Locate and identify every blood parasite.
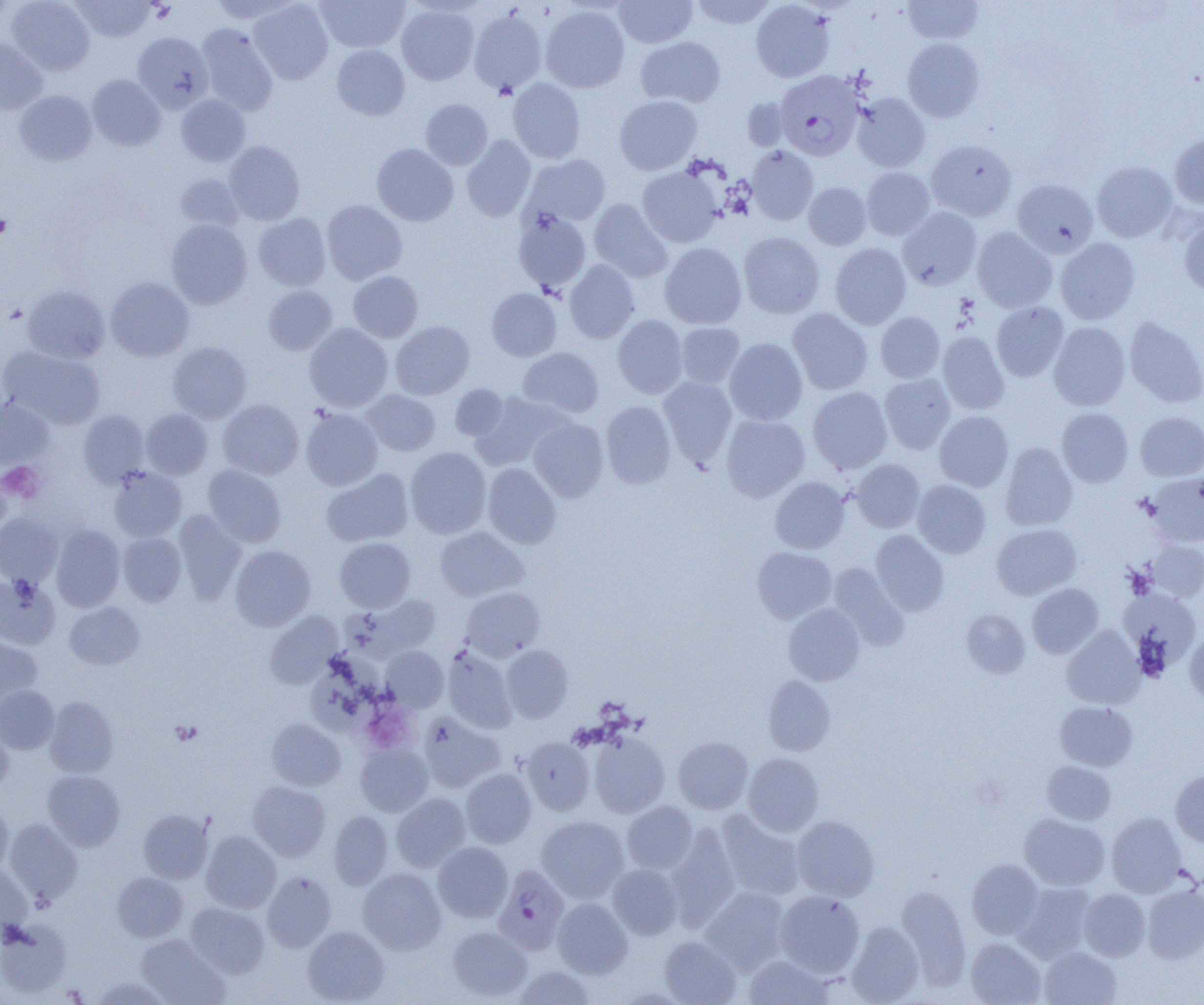
Approximate bounding boxes as [x1, y1, x2, y2] in pixels.
Plasmodium falciparum-infected red blood cells: [778, 76, 867, 165], [493, 865, 570, 954].
No Plasmodium ovale, Plasmodium malariae, Plasmodium vivax, Babesia divergens, or Trypanosoma brucei observed.

Summary:
  - Platelet locations: [149, 2, 175, 21], [0, 213, 11, 240], [1, 461, 44, 502], [169, 719, 203, 746]
  - Uninfected red blood cell locations: [7, 0, 95, 75], [71, 0, 155, 42], [209, 0, 301, 22], [248, 0, 333, 85], [316, 0, 409, 52], [614, 0, 697, 48], [689, 0, 778, 29], [751, 0, 834, 82], [902, 0, 983, 44], [396, 4, 479, 85], [540, 5, 630, 92], [468, 9, 547, 95], [196, 24, 278, 115], [133, 32, 213, 112], [635, 36, 726, 107], [902, 37, 985, 122], [0, 39, 46, 115], [332, 44, 410, 120], [87, 74, 166, 151], [507, 78, 586, 163], [14, 90, 97, 166], [851, 92, 930, 172], [176, 94, 250, 166], [614, 95, 702, 175], [742, 97, 793, 151], [420, 98, 493, 170], [461, 135, 535, 221], [1170, 135, 1204, 208], [224, 140, 305, 225], [926, 140, 1017, 221], [372, 143, 458, 226], [746, 145, 819, 225], [525, 154, 611, 227], [1092, 161, 1177, 242], [637, 166, 723, 247], [862, 167, 935, 240], [175, 174, 245, 232], [1013, 179, 1098, 256], [803, 182, 871, 250], [589, 199, 672, 282], [321, 200, 407, 284], [897, 207, 982, 290], [512, 209, 591, 293], [253, 212, 331, 291], [1179, 218, 1204, 294], [166, 220, 252, 309], [972, 227, 1056, 312], [738, 232, 825, 319], [1056, 237, 1140, 324], [659, 242, 747, 329], [830, 243, 911, 329], [564, 259, 640, 343], [348, 271, 423, 342], [106, 277, 194, 361], [23, 284, 110, 364], [263, 285, 337, 355], [487, 288, 562, 361], [991, 302, 1069, 381], [787, 308, 873, 395], [875, 311, 945, 383], [612, 314, 688, 398], [1124, 316, 1204, 407], [390, 321, 474, 399], [675, 322, 745, 388], [1049, 322, 1130, 411], [304, 323, 393, 412], [937, 332, 1009, 414], [725, 338, 808, 425], [168, 342, 251, 423], [1, 346, 105, 430], [517, 347, 604, 419], [879, 373, 955, 453], [658, 376, 737, 465], [450, 384, 510, 442], [808, 386, 892, 473], [361, 389, 440, 456], [469, 392, 563, 470], [0, 398, 54, 470], [218, 399, 303, 479], [601, 400, 676, 489], [301, 407, 382, 491], [141, 408, 213, 479], [1057, 408, 1133, 487], [78, 410, 149, 486], [934, 411, 1013, 491], [1135, 411, 1204, 481], [721, 414, 809, 502], [529, 417, 609, 502], [1000, 443, 1078, 530], [405, 446, 491, 538], [851, 459, 925, 532], [483, 463, 561, 549], [203, 464, 287, 547], [108, 467, 187, 542], [321, 468, 414, 547], [1145, 473, 1204, 547], [770, 476, 850, 554], [912, 480, 991, 558], [173, 510, 246, 603], [0, 513, 62, 586], [51, 524, 125, 611], [991, 524, 1081, 600], [435, 527, 528, 601], [871, 529, 950, 616], [118, 532, 186, 606], [334, 537, 416, 612], [1145, 540, 1204, 601], [230, 545, 315, 631], [752, 547, 837, 623], [828, 563, 909, 650], [0, 574, 61, 649], [1027, 583, 1103, 658], [461, 587, 545, 661], [1120, 589, 1201, 676], [359, 594, 441, 659], [64, 602, 144, 670], [783, 603, 865, 685], [962, 609, 1030, 678], [265, 611, 343, 687], [1061, 626, 1144, 710], [1185, 629, 1204, 705], [0, 636, 42, 710], [381, 645, 449, 711], [501, 645, 573, 721], [308, 647, 382, 731], [442, 647, 517, 732], [762, 675, 836, 755], [0, 685, 59, 754], [45, 697, 119, 777], [1054, 701, 1138, 771], [419, 712, 505, 793], [266, 719, 345, 790], [0, 724, 13, 796], [588, 731, 670, 818], [673, 736, 753, 814], [521, 737, 595, 815], [356, 743, 433, 816], [744, 753, 823, 836], [1042, 761, 1116, 825], [461, 768, 536, 848], [1170, 768, 1204, 847], [43, 770, 125, 850], [248, 781, 330, 861], [391, 792, 471, 871], [623, 801, 698, 874], [0, 803, 12, 875], [138, 809, 212, 883], [329, 810, 393, 889], [716, 810, 804, 901], [1107, 813, 1186, 897], [1019, 814, 1110, 890], [792, 815, 880, 902], [536, 816, 629, 902], [4, 818, 83, 904], [665, 825, 740, 928], [201, 831, 281, 913], [433, 841, 513, 922], [967, 859, 1043, 939], [0, 864, 33, 937], [608, 864, 683, 939], [358, 868, 445, 954], [112, 872, 188, 942], [262, 872, 336, 952], [1015, 882, 1096, 961], [895, 885, 971, 989], [1142, 885, 1204, 963], [702, 886, 791, 973], [1079, 888, 1151, 961], [775, 890, 865, 977], [553, 898, 633, 978], [186, 903, 269, 978], [0, 920, 72, 997], [846, 921, 925, 1004], [302, 926, 390, 1004], [447, 926, 532, 1001], [137, 934, 230, 1005], [659, 935, 740, 1005], [966, 938, 1046, 1005], [1039, 946, 1121, 1005], [743, 954, 834, 1004], [513, 965, 596, 1004], [92, 975, 170, 1005]
  - Slide-level diagnosis: Plasmodium falciparum
  - Preparation: thin blood film
  - Magnification: 1000x
  - Image size: 1204×1005 pixels
  - Field of view: single
  - Modality: light microscopy